Name the blood parasite species.
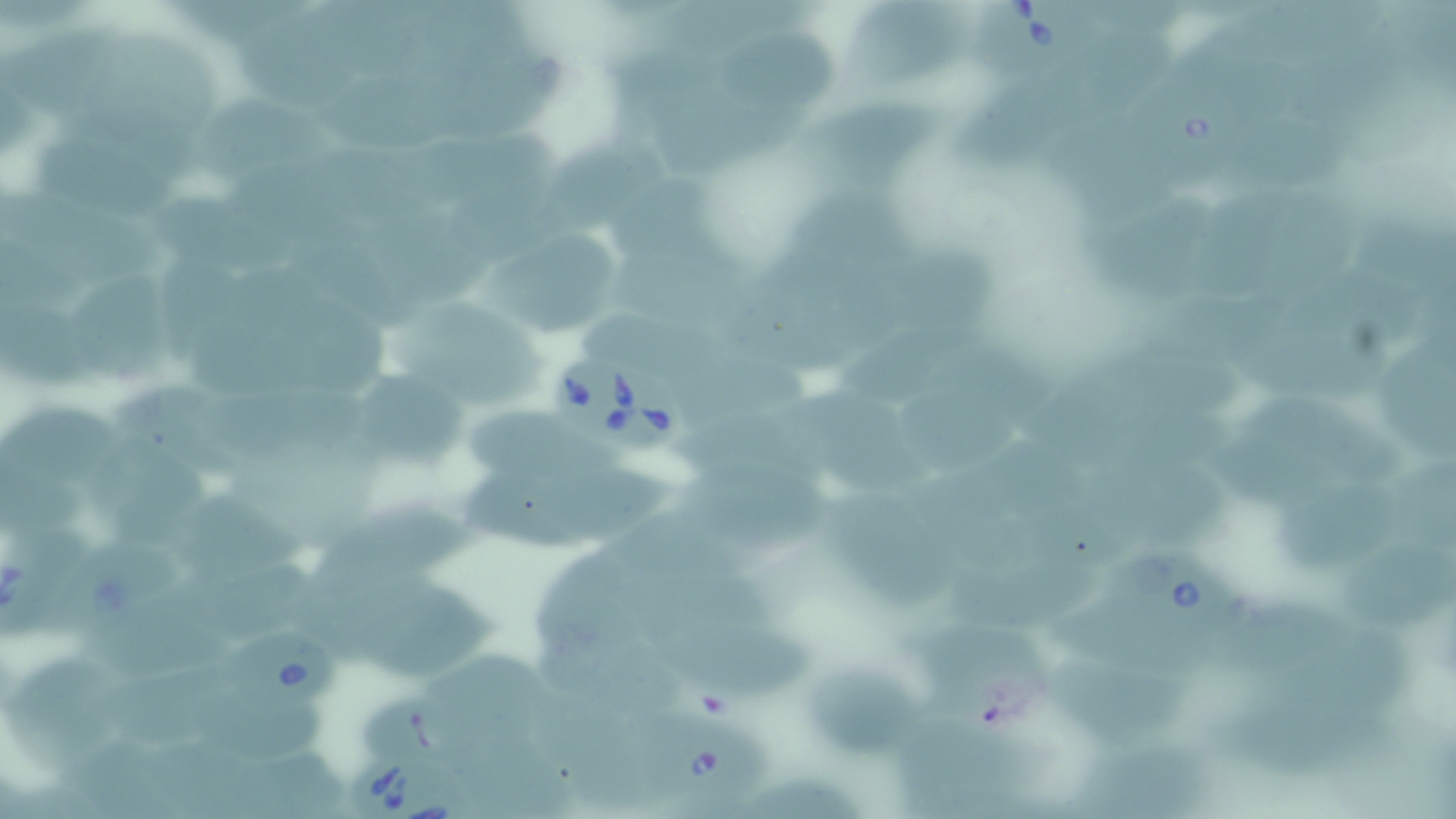

Babesia divergens.

uninfected_red_blood_cell_locations: 'approximate bounding boxes as named x1/y1/x2/y2 corners in pixels: (x1=170, y1=0, x2=314, y2=48), (x1=1229, y1=2, x2=1398, y2=70), (x1=843, y1=9, x2=969, y2=85), (x1=11, y1=14, x2=110, y2=116), (x1=248, y1=19, x2=390, y2=109), (x1=728, y1=21, x2=843, y2=103), (x1=1064, y1=29, x2=1177, y2=109), (x1=105, y1=35, x2=227, y2=132), (x1=453, y1=42, x2=572, y2=141), (x1=615, y1=46, x2=735, y2=133), (x1=347, y1=82, x2=477, y2=152), (x1=959, y1=84, x2=1056, y2=174), (x1=84, y1=92, x2=197, y2=183), (x1=652, y1=93, x2=816, y2=183), (x1=200, y1=97, x2=339, y2=187), (x1=804, y1=98, x2=956, y2=188), (x1=558, y1=124, x2=673, y2=223), (x1=36, y1=125, x2=178, y2=220), (x1=476, y1=127, x2=567, y2=254), (x1=1232, y1=127, x2=1349, y2=191), (x1=1048, y1=132, x2=1182, y2=227), (x1=340, y1=144, x2=457, y2=235), (x1=251, y1=160, x2=390, y2=271), (x1=614, y1=176, x2=721, y2=261), (x1=1196, y1=180, x2=1294, y2=306), (x1=784, y1=183, x2=926, y2=261), (x1=0, y1=186, x2=168, y2=288), (x1=159, y1=190, x2=291, y2=275), (x1=1105, y1=192, x2=1221, y2=305), (x1=1276, y1=200, x2=1367, y2=301), (x1=1345, y1=207, x2=1456, y2=309), (x1=626, y1=225, x2=757, y2=314), (x1=395, y1=226, x2=497, y2=313), (x1=4, y1=237, x2=94, y2=313), (x1=493, y1=239, x2=621, y2=337), (x1=910, y1=246, x2=1001, y2=329), (x1=739, y1=258, x2=833, y2=380), (x1=257, y1=270, x2=387, y2=387), (x1=76, y1=275, x2=174, y2=396), (x1=194, y1=293, x2=314, y2=406), (x1=403, y1=298, x2=547, y2=419), (x1=8, y1=306, x2=99, y2=399), (x1=580, y1=312, x2=708, y2=363), (x1=854, y1=312, x2=984, y2=393), (x1=1091, y1=324, x2=1259, y2=399), (x1=1371, y1=334, x2=1456, y2=464), (x1=928, y1=338, x2=1048, y2=403), (x1=701, y1=368, x2=820, y2=419), (x1=1050, y1=373, x2=1186, y2=442), (x1=118, y1=375, x2=256, y2=470), (x1=910, y1=379, x2=1027, y2=470), (x1=367, y1=385, x2=465, y2=473), (x1=1263, y1=389, x2=1406, y2=485), (x1=7, y1=396, x2=131, y2=497), (x1=786, y1=396, x2=938, y2=497), (x1=469, y1=399, x2=611, y2=475), (x1=1203, y1=415, x2=1357, y2=499), (x1=967, y1=439, x2=1097, y2=529), (x1=91, y1=443, x2=214, y2=529), (x1=562, y1=458, x2=688, y2=536), (x1=1102, y1=460, x2=1239, y2=550), (x1=1397, y1=466, x2=1456, y2=566), (x1=689, y1=468, x2=841, y2=556), (x1=1279, y1=471, x2=1412, y2=560), (x1=469, y1=476, x2=606, y2=554), (x1=184, y1=491, x2=310, y2=570), (x1=316, y1=493, x2=483, y2=577), (x1=847, y1=501, x2=949, y2=609), (x1=625, y1=517, x2=756, y2=580), (x1=299, y1=546, x2=440, y2=625), (x1=538, y1=550, x2=661, y2=658), (x1=956, y1=554, x2=1103, y2=629), (x1=1339, y1=554, x2=1456, y2=635), (x1=172, y1=556, x2=314, y2=627), (x1=358, y1=577, x2=519, y2=675), (x1=664, y1=582, x2=786, y2=652), (x1=1229, y1=597, x2=1349, y2=668), (x1=91, y1=605, x2=233, y2=694), (x1=1077, y1=605, x2=1225, y2=687), (x1=1249, y1=625, x2=1417, y2=711), (x1=924, y1=633, x2=1054, y2=727), (x1=666, y1=635, x2=827, y2=700), (x1=528, y1=637, x2=702, y2=710), (x1=13, y1=648, x2=133, y2=765), (x1=819, y1=655, x2=926, y2=765), (x1=442, y1=656, x2=570, y2=727), (x1=122, y1=662, x2=241, y2=734), (x1=1064, y1=669, x2=1204, y2=751), (x1=355, y1=679, x2=462, y2=765), (x1=208, y1=690, x2=339, y2=755), (x1=1223, y1=690, x2=1392, y2=781), (x1=551, y1=698, x2=674, y2=812), (x1=457, y1=713, x2=578, y2=813), (x1=905, y1=719, x2=1031, y2=819), (x1=1086, y1=734, x2=1225, y2=812), (x1=741, y1=767, x2=869, y2=819)'
babesia_divergens_infected_red_blood_cell_locations: 'approximate bounding boxes as named x1/y1/x2/y2 corners in pixels: (x1=975, y1=3, x2=1110, y2=80), (x1=1140, y1=80, x2=1247, y2=176), (x1=551, y1=354, x2=701, y2=454), (x1=0, y1=525, x2=88, y2=639), (x1=40, y1=530, x2=188, y2=645), (x1=1107, y1=541, x2=1251, y2=644), (x1=225, y1=620, x2=339, y2=713), (x1=647, y1=717, x2=770, y2=801), (x1=353, y1=751, x2=480, y2=817)'
field_of_view: one of a larger specimen
modality: optical microscopy
magnification: 1000x
preparation: thin blood smear
stain: May-Grünwald-Giemsa
image_size: 1456×819 pixels